Outline each blood parasite and name the species.
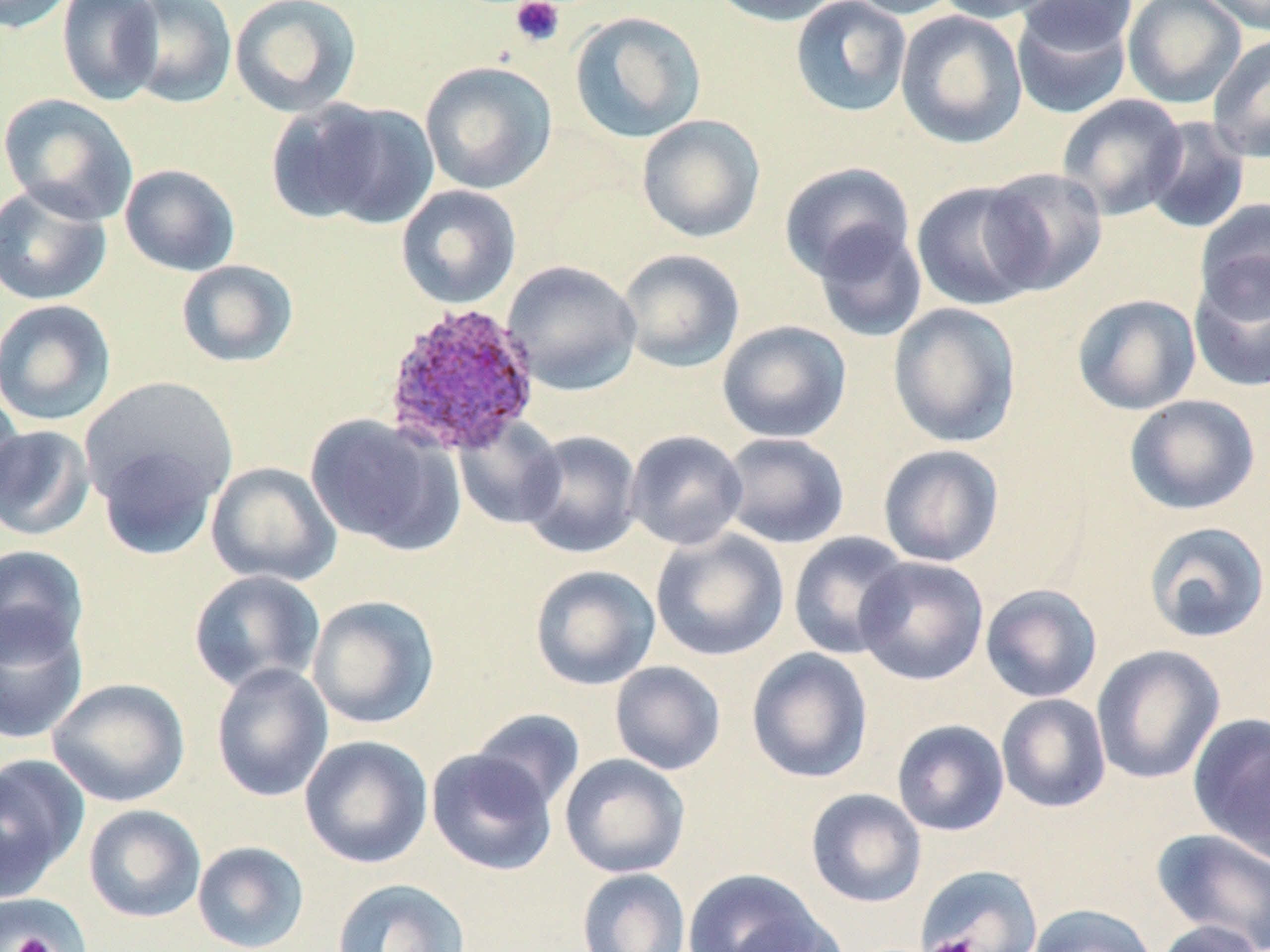

Approximate bounding boxes as [x1, y1, x2, y2] in pixels.
Plasmodium ovale-infected red blood cells: [381, 301, 541, 457].
No Plasmodium falciparum, Plasmodium malariae, Plasmodium vivax, Babesia divergens, or Trypanosoma brucei observed.

{
  "slide_level_diagnosis": "Plasmodium ovale",
  "platelet_locations": "approximate bounding boxes as [x1, y1, x2, y2] in pixels: [509, 0, 565, 48], [9, 933, 56, 951], [929, 935, 976, 952]",
  "magnification": "1000x",
  "image_size": "1270×952 pixels",
  "modality": "light microscopy",
  "stain": "May-Grünwald-Giemsa",
  "field_of_view": "one of a larger specimen",
  "preparation": "thin blood film",
  "uninfected_red_blood_cell_locations": "approximate bounding boxes as [x1, y1, x2, y2] in pixels: [0, 0, 75, 34], [57, 0, 164, 105], [123, 0, 238, 108], [229, 0, 362, 118], [708, 0, 845, 27], [790, 0, 912, 118], [841, 0, 964, 19], [935, 0, 1061, 23], [1015, 0, 1139, 55], [1122, 0, 1246, 108], [1199, 0, 1270, 35], [1011, 5, 1133, 119], [568, 10, 707, 143], [895, 10, 1028, 149], [1207, 34, 1270, 163], [420, 60, 558, 195], [0, 93, 138, 225], [1056, 94, 1189, 221], [287, 99, 440, 229], [636, 114, 766, 244], [1142, 116, 1251, 235], [779, 162, 915, 282], [119, 164, 240, 277], [980, 167, 1108, 295], [910, 180, 1044, 311], [0, 184, 112, 306], [396, 184, 522, 309], [1194, 198, 1270, 320], [812, 223, 928, 343], [617, 249, 745, 374], [175, 259, 299, 368], [502, 260, 642, 396], [1189, 262, 1270, 393], [1072, 293, 1202, 415], [0, 299, 117, 426], [888, 302, 1022, 449], [717, 320, 852, 443], [80, 376, 239, 510], [0, 388, 26, 514], [1124, 394, 1261, 516], [304, 414, 459, 553], [454, 416, 566, 529], [0, 424, 96, 541], [519, 430, 643, 559], [624, 430, 748, 550], [718, 432, 850, 549], [96, 444, 219, 560], [877, 444, 1005, 568], [205, 462, 341, 587], [1142, 521, 1270, 644], [651, 529, 790, 662], [787, 531, 912, 660], [0, 545, 89, 665], [854, 556, 989, 686], [529, 564, 661, 691], [188, 569, 325, 694], [980, 584, 1103, 703], [307, 594, 440, 729], [0, 610, 88, 745], [1091, 644, 1225, 785], [746, 647, 873, 784], [609, 661, 726, 775], [210, 662, 333, 802], [47, 677, 190, 807], [996, 693, 1112, 813], [469, 709, 586, 813], [1188, 712, 1270, 861], [891, 719, 1010, 836], [299, 735, 433, 869], [426, 749, 558, 876], [0, 753, 89, 900], [558, 754, 691, 878], [805, 788, 927, 908], [83, 804, 206, 923], [1151, 828, 1270, 951], [192, 840, 310, 952], [916, 864, 1043, 951], [576, 868, 691, 952], [682, 868, 831, 952], [330, 878, 471, 952], [1, 893, 93, 951], [1027, 903, 1158, 952], [1153, 920, 1266, 952]"
}